State the preparation type.
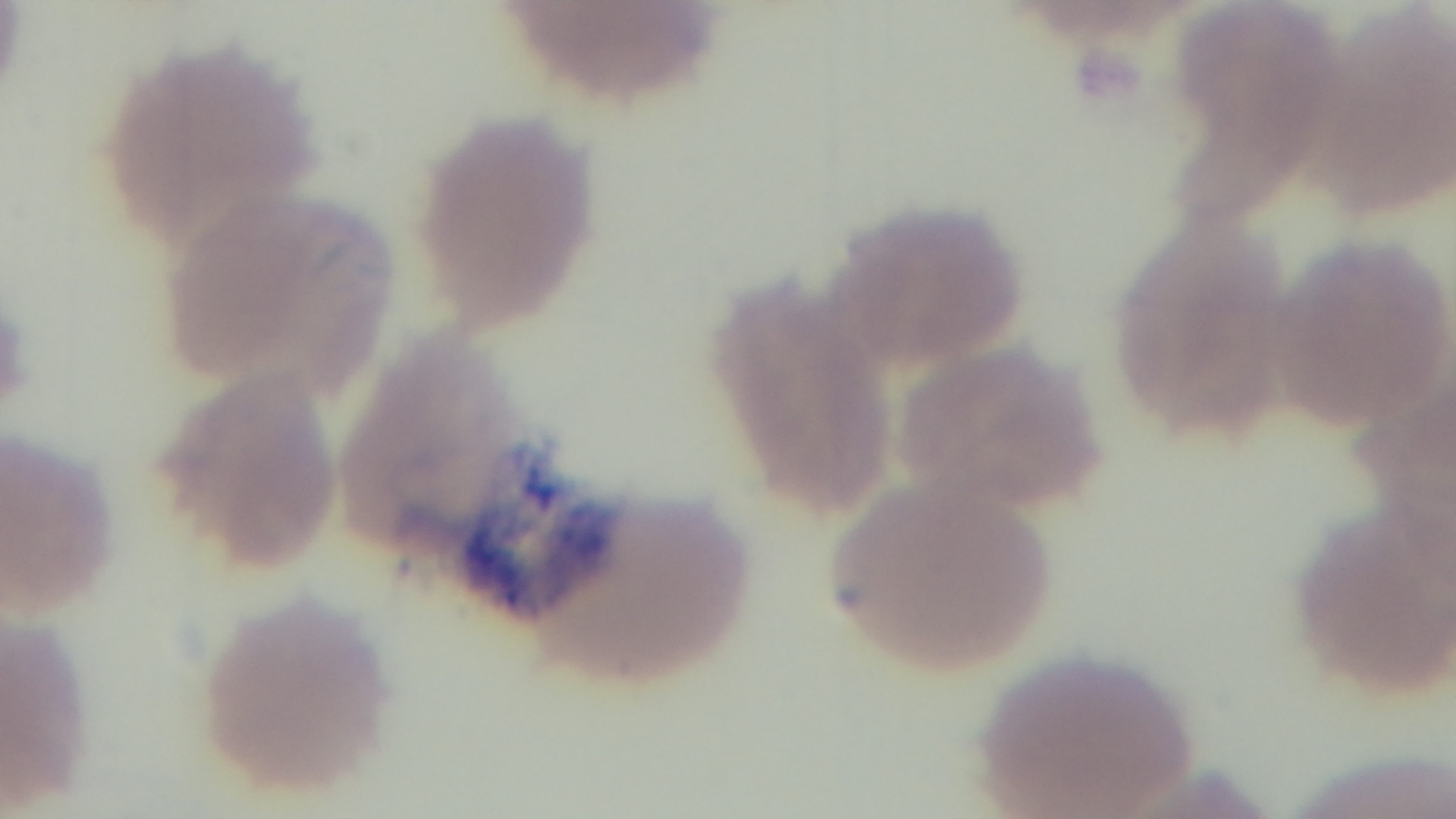
It is a thin blood film.

Summary:
  - Capture: mounted 4K digital camera
  - Malaria status: positive
  - Modality: light microscopy
  - Objective: 100x oil immersion
  - Stain: Giemsa
  - Field of view: single